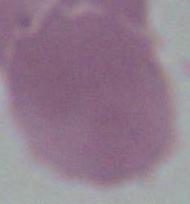
An erythrocyte is shown. Photomicrograph. 1000x magnification.